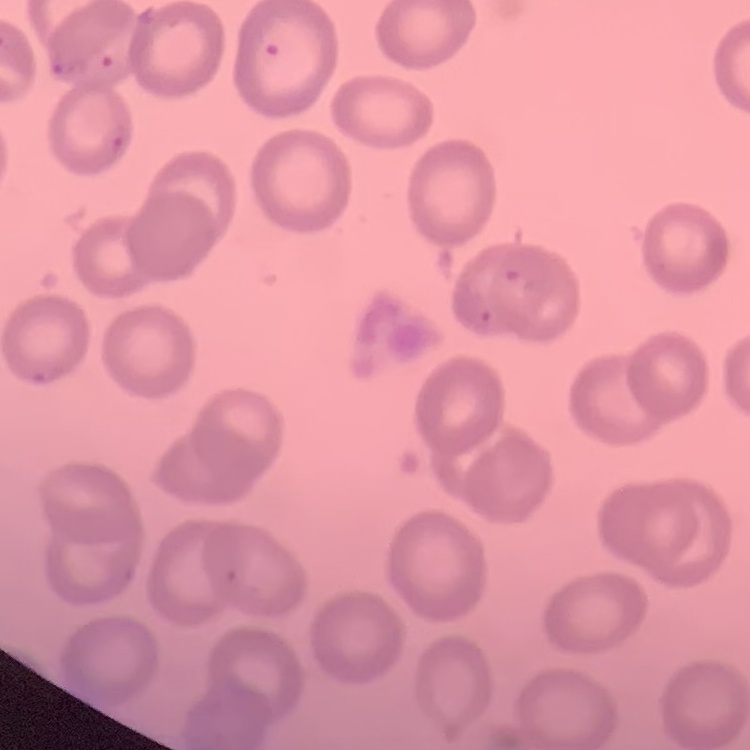

{
  "erythrocyte_morphology": "no rouleaux formation",
  "preparation": "thin blood film",
  "stain": "Field's or Giemsa",
  "image_type": "square crop of a larger photomicrograph"
}